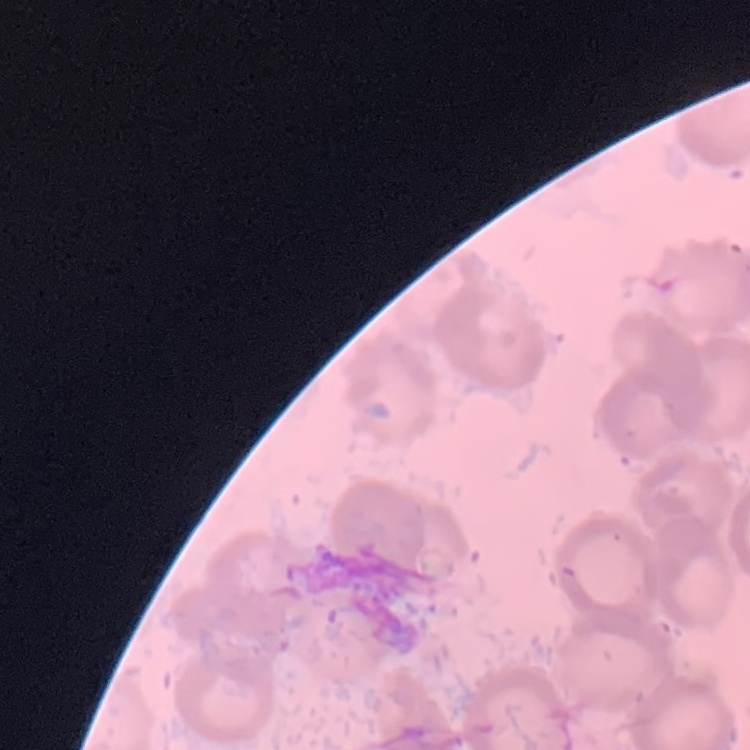 The erythrocytes show no rouleaux formation. Field's or Giemsa stain. Square crop of a larger photomicrograph. Thin peripheral smear.